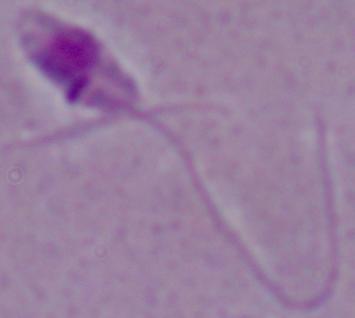

Summary:
  - Identification: Leishmania
  - Magnification: 1000x
  - Modality: micrograph